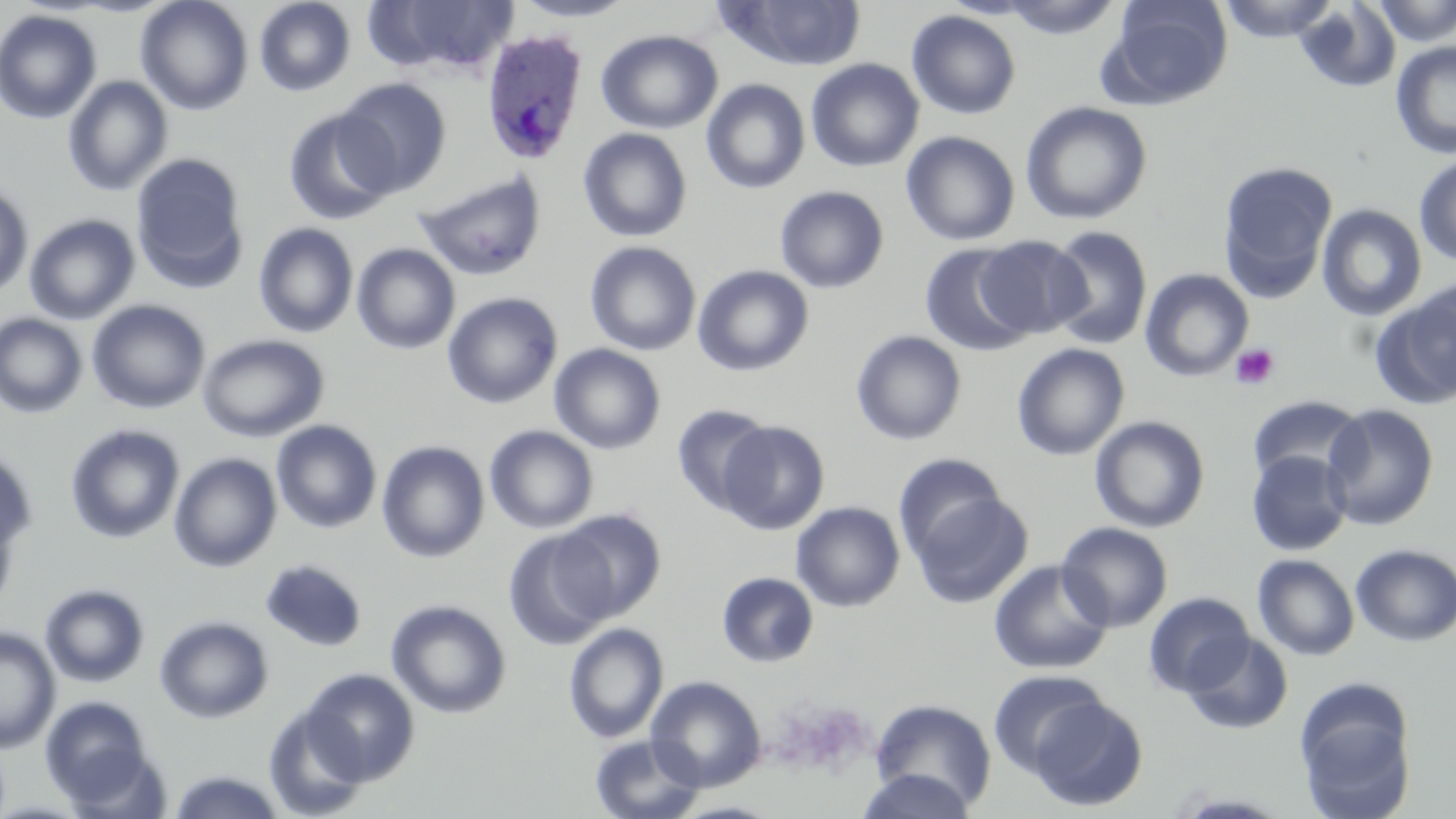
Approximate bounding boxes as (x1,y1)-(x2,y2) corner pairs in pixels. Platelet locations: (1230,343)-(1280,390). Uninfected red blood cell locations: (135,0)-(254,115), (510,0)-(637,22), (1000,0)-(1121,39), (1105,0)-(1233,108), (1217,0)-(1340,43), (1372,0)-(1456,46), (253,1)-(356,97), (364,1)-(520,79), (718,1)-(868,72), (1294,1)-(1402,93), (0,9)-(102,124), (907,10)-(1021,120), (596,29)-(723,134), (1390,41)-(1456,160), (805,58)-(924,172), (62,76)-(173,196), (336,78)-(452,196), (701,78)-(810,194), (1020,101)-(1153,225), (282,107)-(401,226), (578,127)-(692,242), (901,131)-(1020,245), (131,153)-(250,292), (1414,154)-(1456,267), (1218,160)-(1338,300), (413,169)-(548,281), (0,182)-(33,299), (774,185)-(890,294), (1316,203)-(1427,321), (24,214)-(140,325), (253,222)-(359,338), (1044,225)-(1153,351), (975,234)-(1091,339), (584,241)-(701,356), (352,243)-(460,354), (920,243)-(1034,357), (692,265)-(814,377), (1140,269)-(1253,381), (1370,287)-(1456,410), (442,292)-(562,409), (87,299)-(210,414), (0,313)-(88,418), (850,330)-(967,446), (197,333)-(329,442), (1011,342)-(1130,461), (549,344)-(666,454), (1246,394)-(1367,486), (672,403)-(774,516), (1321,403)-(1439,530), (1090,415)-(1211,533), (271,419)-(382,533), (717,420)-(830,534), (65,423)-(185,544), (484,425)-(599,533), (376,441)-(490,562), (63,443)-(280,558), (0,445)-(37,555), (1246,450)-(1353,556), (168,452)-(281,572), (894,454)-(1007,560), (911,492)-(1032,608), (790,501)-(905,612), (0,502)-(19,620), (555,508)-(667,621), (1057,523)-(1173,633), (503,529)-(617,650), (1351,544)-(1456,646), (1252,554)-(1360,660), (260,558)-(368,652), (988,559)-(1114,674), (717,571)-(819,668), (40,583)-(150,688), (1143,591)-(1255,697), (386,599)-(511,718), (154,615)-(274,724), (564,623)-(668,743), (0,625)-(61,754), (1181,632)-(1294,735), (301,668)-(419,786), (987,668)-(1109,777), (646,676)-(767,791), (1294,680)-(1417,819), (40,694)-(157,808), (1027,696)-(1148,811), (869,698)-(998,811), (263,703)-(373,819), (589,733)-(706,819), (166,769)-(289,818), (854,770)-(977,819). Plasmodium ovale-infected red blood cell locations: (480,28)-(588,163). Slide-level diagnosis: Plasmodium ovale. May-Grünwald-Giemsa-stained preparation. Image is 1456×819 pixels. Captured at 1000x magnification. Thin blood smear. One field of a larger specimen. Light microscopy.